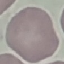

malaria_status: uninfected
stain: Giemsa
image_type: cell patch, automatically extracted from a larger field of view and resized to 64 × 64 pixels
capture: smartphone camera at the microscope eyepiece
preparation: thin smear